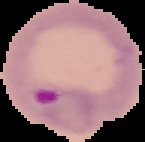
image_type: cell region segmented out of the field of view; surrounding area masked to black
result: malaria parasites detected
image_size: 145×142 pixels
preparation: thin blood smear